Identify the cell.
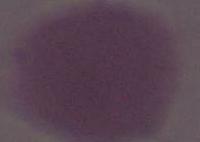
An erythrocyte.

modality: micrograph
magnification: 1000x